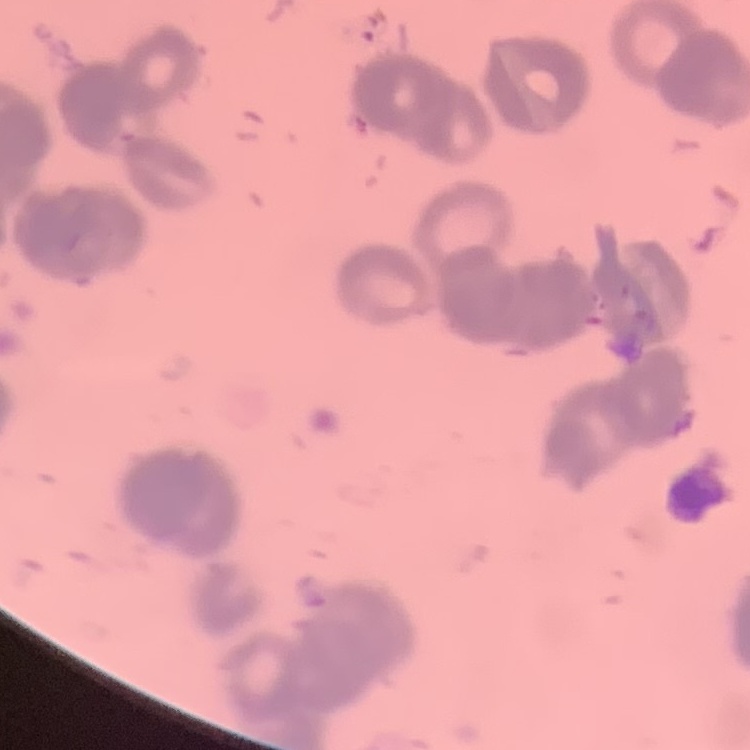
red blood cell morphology = rouleaux formation
stain = Field's or Giemsa
preparation = thin peripheral smear
image type = square crop of a larger photomicrograph